Comment on the morphology of the red blood cells.
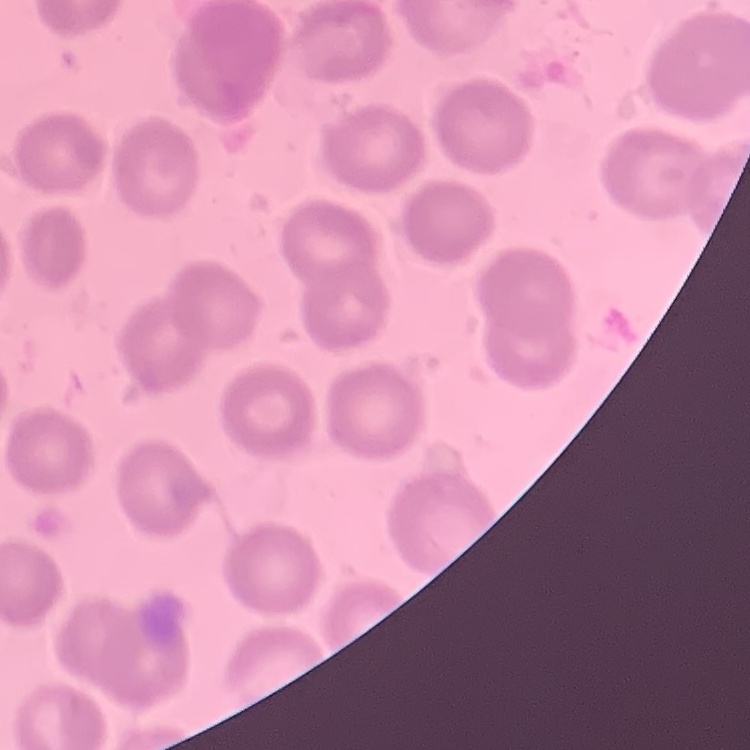
No rouleaux formation.

Summary:
  - Stain: Field's or Giemsa
  - Preparation: thin blood film
  - Image type: one tile cut from a larger photomicrograph